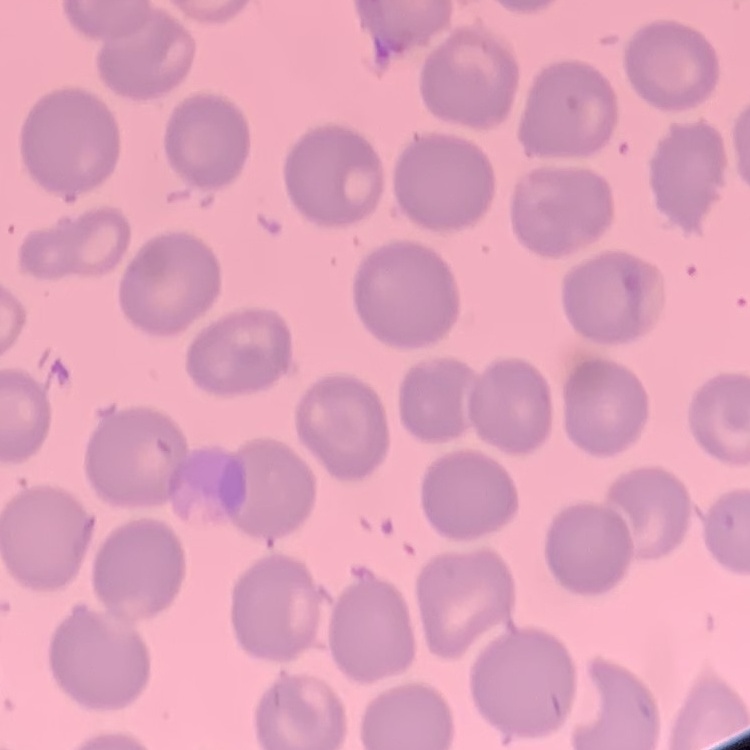

erythrocyte_morphology: no rouleaux formation
stain: Field's or Giemsa
image_type: square crop of a larger photomicrograph
preparation: thin blood smear